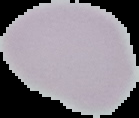
image size = 139×118 pixels
image type = cell region segmented out of the field of view; surrounding area masked to black
preparation = thin blood film
malaria status = uninfected